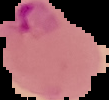
The area outside the segmented cell region is set to black. From a thin blood smear. Malaria status: parasitized. Image is 109×100 pixels.